Identify the parasite.
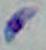
This is Toxoplasma gondii.

magnification = 1000x
modality = micrograph